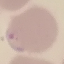
malaria_status: parasitized
preparation: thin smear
image_type: automatically extracted cell patch, resized to 64 × 64 pixels
stain: Giemsa
capture: smartphone through the microscope eyepiece